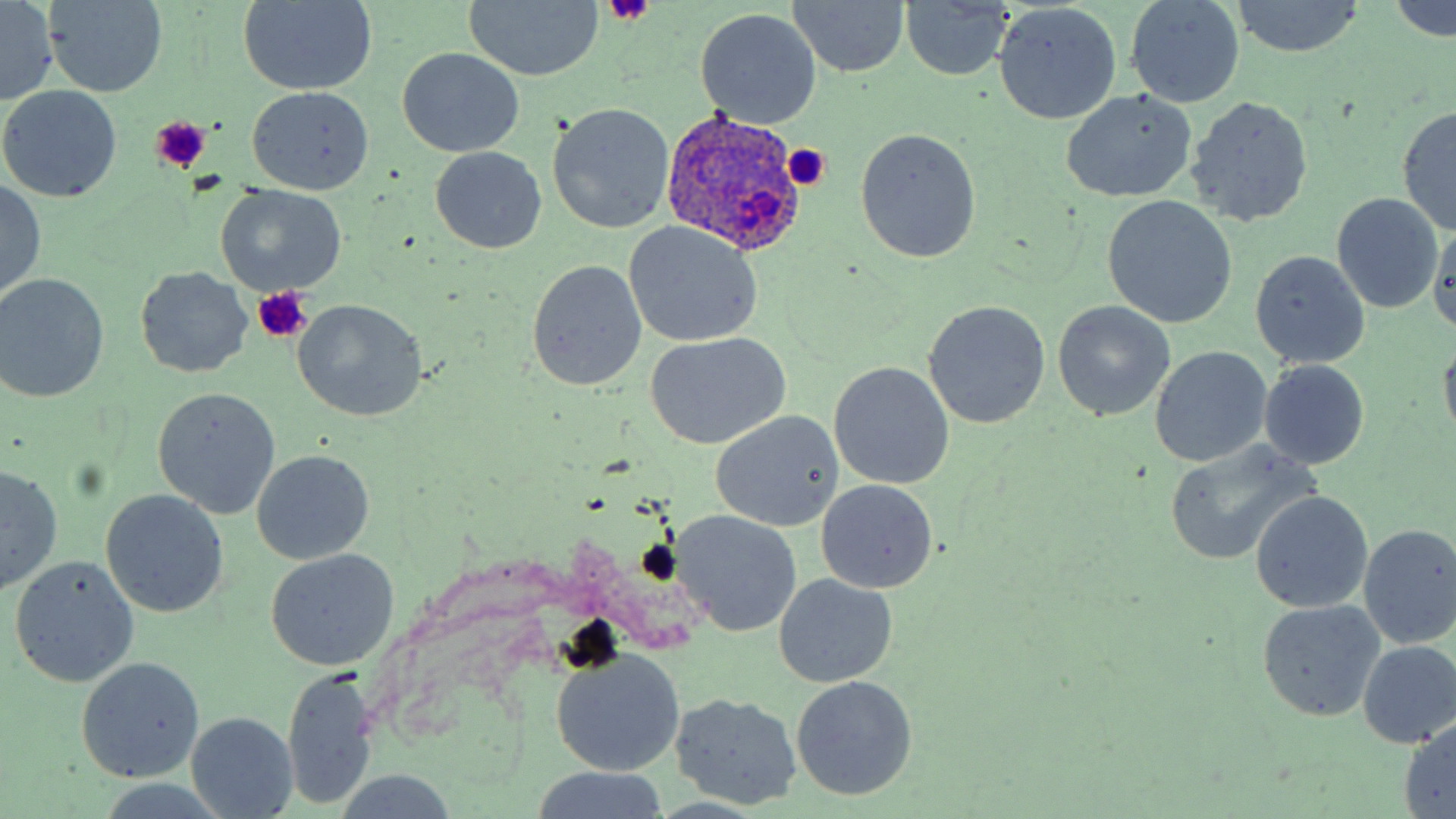
slide_level_diagnosis: Plasmodium ovale
platelet_locations: 'approximate bounding boxes as (x1, y1, x2, y2) in pixels: (604, 0, 655, 26), (149, 117, 213, 174), (783, 145, 834, 188), (252, 287, 311, 341)'
magnification: 1000x
modality: light microscopy
preparation: thin blood smear
stain: May-Grünwald-Giemsa
plasmodium_ovale_infected_red_blood_cell_locations: 'approximate bounding boxes as (x1, y1, x2, y2) in pixels: (660, 109, 809, 256)'
uninfected_red_blood_cell_locations: 'approximate bounding boxes as (x1, y1, x2, y2) in pixels: (1126, 0, 1244, 108), (1229, 0, 1370, 58), (43, 1, 169, 97), (463, 1, 604, 82), (785, 1, 911, 79), (1388, 1, 1456, 40), (0, 2, 57, 104), (898, 2, 1015, 82), (237, 3, 378, 94), (994, 3, 1122, 124), (694, 8, 822, 128), (398, 48, 525, 158), (0, 86, 123, 202), (247, 86, 373, 195), (1060, 88, 1197, 204), (1188, 96, 1315, 228), (548, 103, 674, 233), (1396, 106, 1456, 234), (855, 128, 981, 262), (430, 148, 546, 254), (0, 180, 46, 299), (215, 185, 347, 295), (1332, 194, 1443, 313), (1101, 195, 1237, 328), (1427, 220, 1456, 339), (624, 221, 763, 346), (1249, 251, 1371, 372), (527, 260, 647, 392), (134, 267, 254, 379), (0, 274, 110, 402), (923, 300, 1050, 429), (292, 301, 426, 422), (1052, 301, 1175, 420), (1437, 333, 1456, 447), (649, 334, 789, 449), (1148, 346, 1272, 468), (830, 361, 955, 490), (1259, 361, 1370, 468), (153, 388, 280, 519), (708, 411, 843, 532), (1164, 439, 1317, 566), (252, 450, 374, 564), (0, 464, 63, 594), (816, 479, 937, 594), (101, 489, 228, 616), (1250, 491, 1373, 614), (673, 512, 800, 636), (1357, 524, 1456, 650), (266, 549, 399, 671), (10, 556, 139, 687), (775, 574, 898, 687), (1254, 600, 1386, 722), (1354, 640, 1456, 749), (551, 649, 685, 775), (76, 657, 204, 782), (280, 671, 382, 810), (791, 675, 918, 800), (669, 693, 804, 810), (186, 712, 299, 817), (1399, 719, 1456, 817), (529, 769, 673, 818), (335, 772, 459, 817)'
field_of_view: single
image_size: 1456×819 pixels